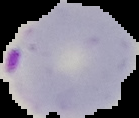 Result: Plasmodium parasites detected. Image is 139×118 pixels. The area outside the segmented cell region is set to black. From a thin blood film.